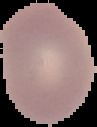
Summary:
  - Image size: 97×127 pixels
  - Preparation: thin blood smear
  - Image type: segmented cell region on a black background
  - Malaria status: uninfected